Report the malaria status of this cell.
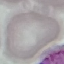

It is uninfected.

Automatically extracted cell patch, resized to 64 × 64 pixels. Thin blood film. Photographed with a smartphone camera at the microscope eyepiece. Giemsa stain.